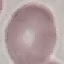
{
  "result": "negative for malaria parasites",
  "stain": "Giemsa",
  "image_type": "automatically extracted cell patch, resized to 64 × 64 pixels",
  "preparation": "thin blood film",
  "capture": "smartphone through the microscope eyepiece"
}